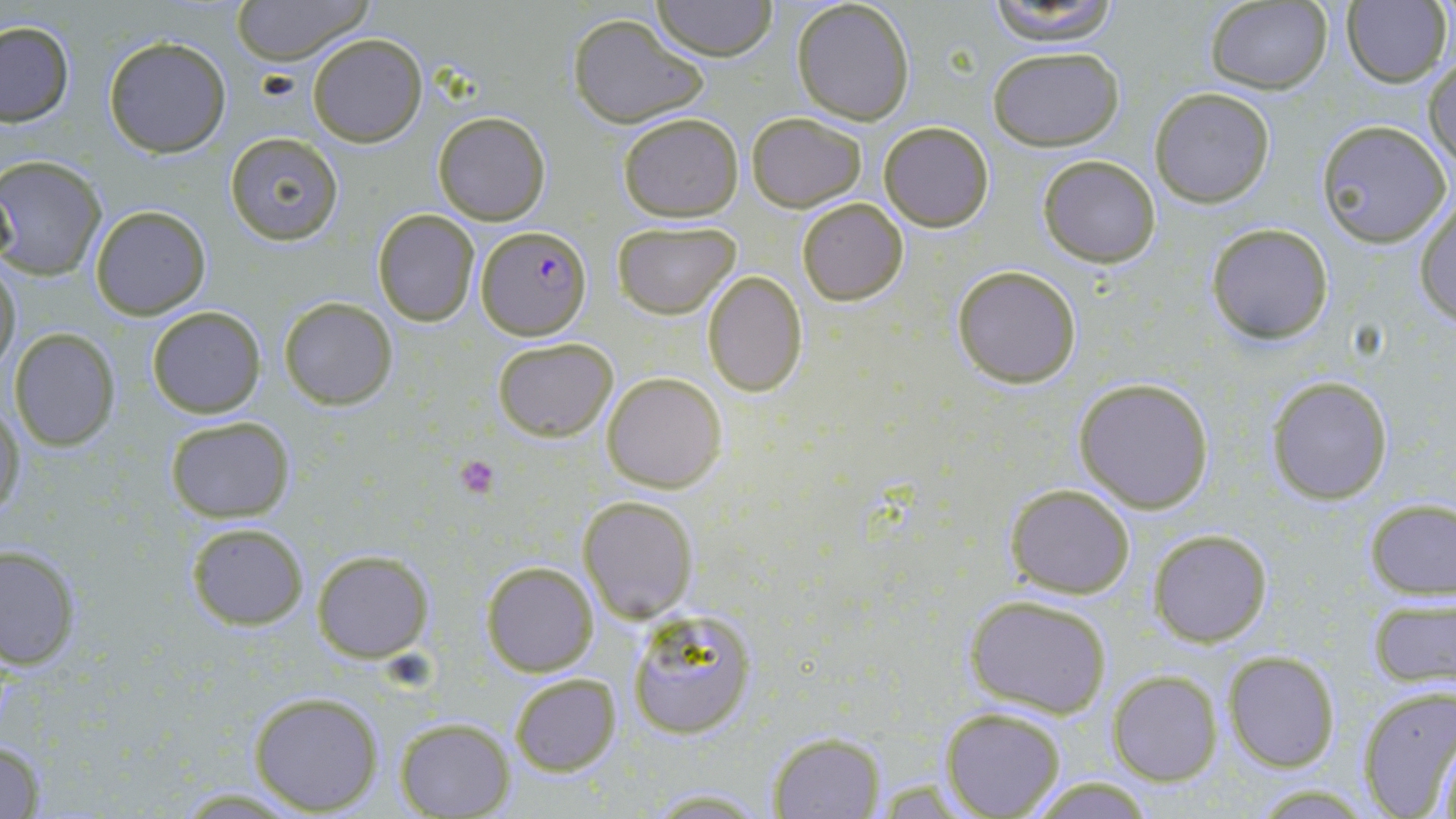
Approximate bounding boxes as (x1,y1)-(x2,y2) corner pairs in pixels. Uninfected red blood cell locations: (230,0)-(373,64), (653,0)-(776,61), (791,0)-(916,125), (982,0)-(1125,45), (1203,2)-(1333,94), (1341,2)-(1451,87), (568,13)-(707,127), (0,22)-(74,126), (307,33)-(428,148), (103,35)-(232,157), (986,45)-(1124,151), (1426,53)-(1456,175), (1149,88)-(1275,208), (432,111)-(551,225), (617,111)-(743,222), (745,112)-(868,211), (1316,119)-(1453,247), (879,120)-(995,232), (224,131)-(343,244), (1036,154)-(1162,266), (0,157)-(107,280), (1414,195)-(1456,326), (797,199)-(908,305), (89,205)-(212,319), (372,209)-(479,326), (612,220)-(741,318), (1206,223)-(1333,346), (0,262)-(22,373), (951,264)-(1082,388), (701,271)-(808,396), (278,297)-(398,408), (146,306)-(266,418), (8,328)-(121,449), (492,337)-(618,440), (601,371)-(728,492), (1266,375)-(1394,504), (1073,378)-(1214,513), (1,404)-(23,522), (164,416)-(295,522), (1004,483)-(1135,598), (578,494)-(698,621), (1364,498)-(1455,599), (186,522)-(309,629), (1148,529)-(1272,647), (1,544)-(80,671), (310,550)-(434,661), (481,561)-(598,677), (1364,593)-(1454,688), (964,596)-(1112,717), (626,608)-(756,739), (1222,649)-(1341,771), (1109,672)-(1222,785), (509,674)-(621,775), (1356,683)-(1455,819), (248,690)-(383,815), (942,707)-(1068,818), (395,716)-(515,818), (770,731)-(885,818), (1432,731)-(1456,819), (0,735)-(49,818), (1021,775)-(1160,817), (636,786)-(777,817). Platelet locations: (456,456)-(498,499). Plasmodium falciparum-infected red blood cell locations: (476,226)-(590,341). Slide-level diagnosis: Plasmodium falciparum. Thin blood smear. May-Grünwald-Giemsa stain. Optical microscopy. One field of a larger specimen. Captured at 1000x magnification. Image is 1456×819 pixels.